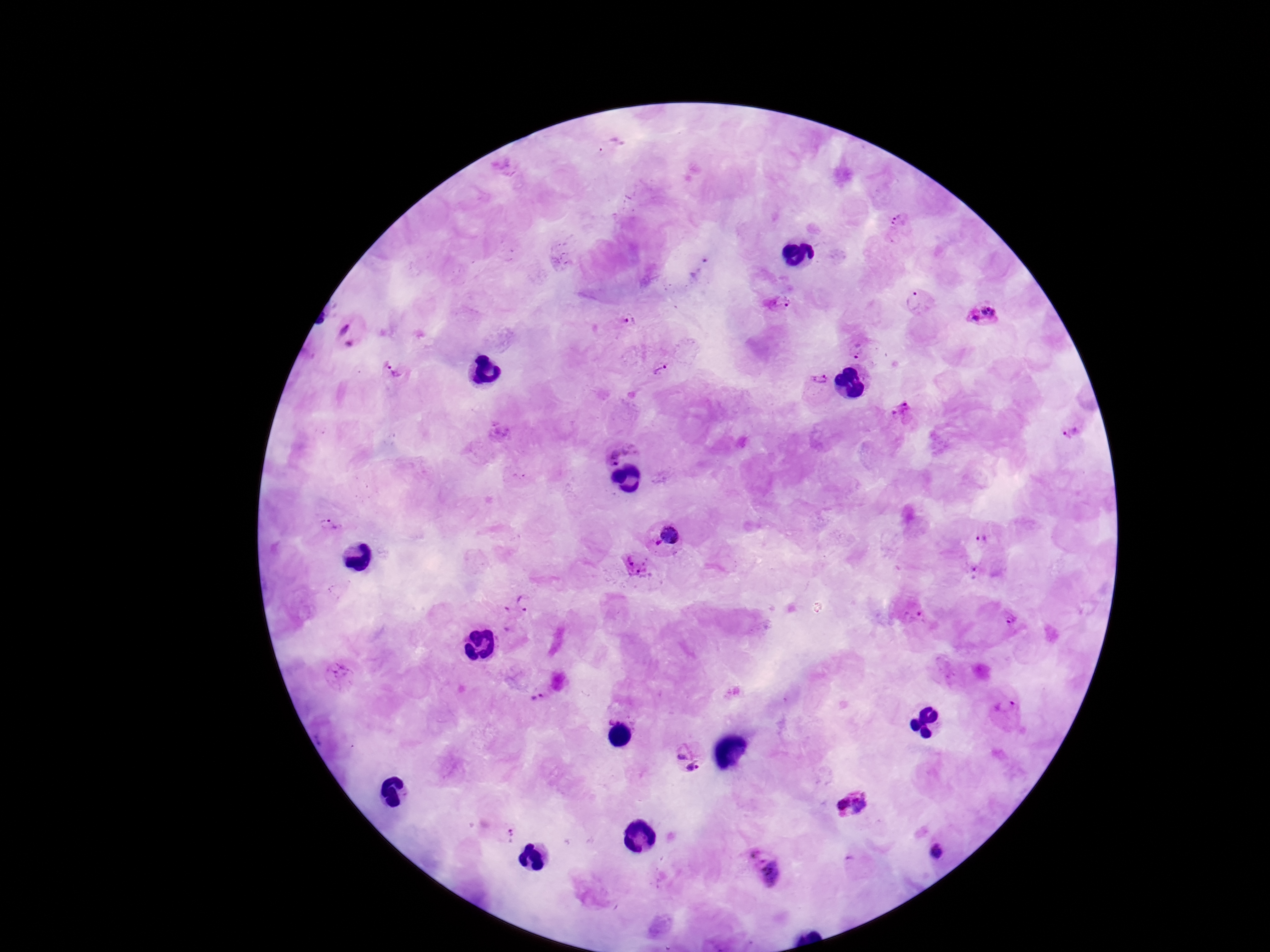
Approximate centers as (x, y) in pixels. Plasmodium parasite locations: (900, 230), (700, 268), (917, 299), (777, 302), (983, 314), (623, 320), (351, 332), (859, 348), (661, 366), (395, 369), (819, 387), (907, 412), (1072, 433), (617, 443), (328, 524), (667, 534), (987, 540), (633, 569), (977, 576), (525, 608), (913, 610), (1009, 620), (541, 692), (1006, 706), (692, 756), (853, 806), (505, 834), (937, 852), (762, 867). One field from this slide. Patient malaria status: infected. Photographed through the microscope eyepiece with a smartphone camera. Giemsa stain. Thick peripheral-blood smear. Image is 1270×952 pixels. 100x magnification.